Classify this cell by malaria status.
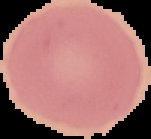

Uninfected.

image_size: 151×139 pixels
preparation: thin blood smear
image_type: segmented cell region on a black background